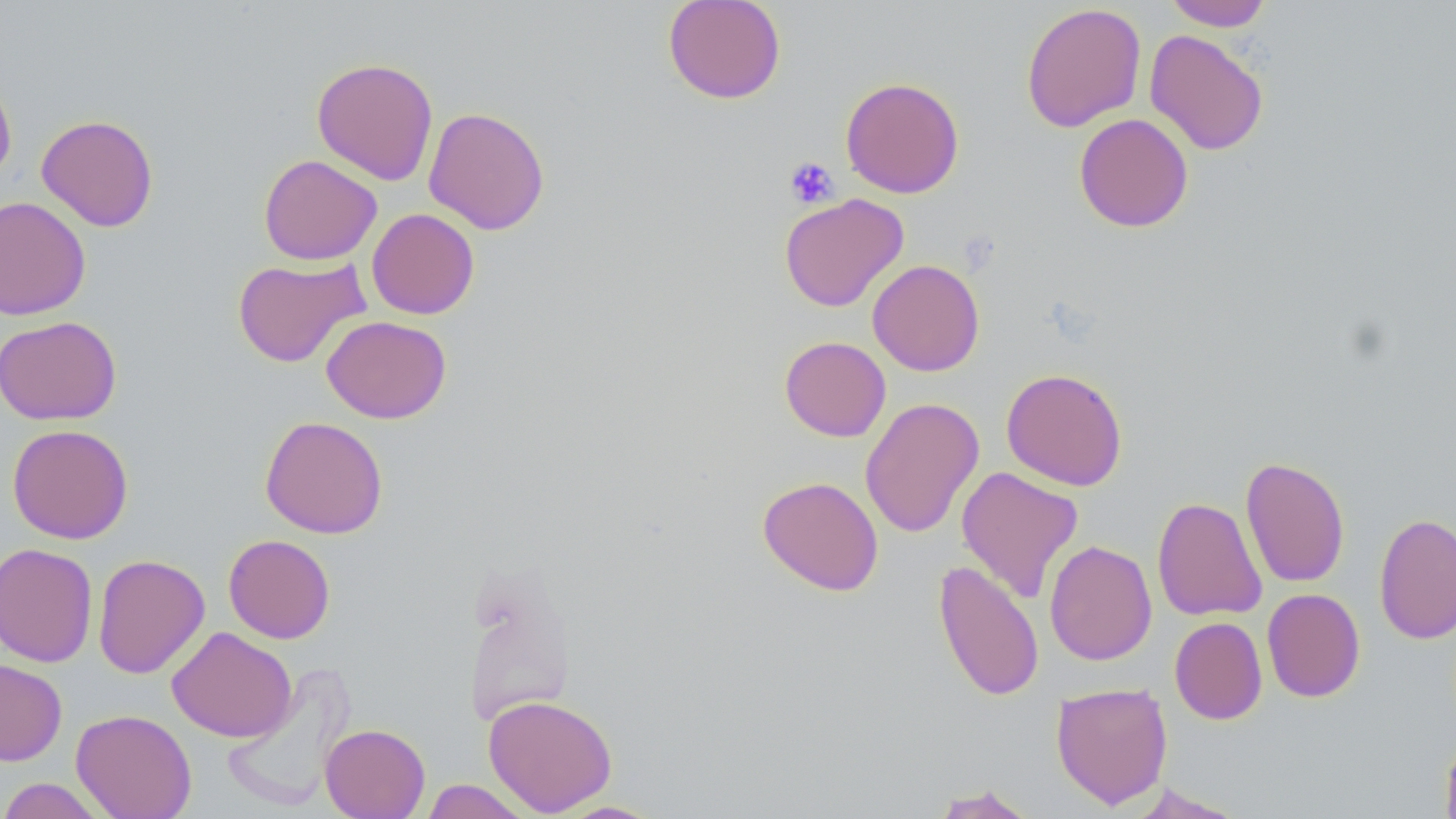
Summary:
  - Coordinate format: approximate bounding boxes as (x1,y1)-(x2,y2) corner pairs in pixels
  - Uninfected red blood cell locations: (662,0)-(786,104), (1163,0)-(1274,31), (1021,2)-(1147,132), (1144,29)-(1270,156), (311,57)-(439,185), (0,72)-(17,185), (840,76)-(965,198), (423,106)-(550,235), (1073,113)-(1194,233), (36,114)-(159,232), (258,154)-(382,265), (779,193)-(909,312), (0,196)-(91,321), (366,208)-(480,319), (232,256)-(369,367), (867,259)-(985,376), (0,315)-(122,425), (321,315)-(452,424), (779,336)-(891,441), (1001,368)-(1128,490), (860,397)-(984,538), (259,415)-(388,539), (7,423)-(133,544), (1240,456)-(1350,588), (956,466)-(1084,603), (757,476)-(884,596), (1152,496)-(1267,621), (1374,512)-(1456,645), (223,534)-(336,643), (1044,540)-(1157,666), (0,542)-(99,668), (92,554)-(210,679), (459,558)-(579,729), (933,560)-(1045,702), (1262,588)-(1366,703), (1169,617)-(1267,725), (167,627)-(297,743), (0,658)-(67,766), (222,668)-(355,812), (1051,681)-(1173,809), (483,694)-(617,816), (71,709)-(197,819), (320,723)-(430,819), (1440,733)-(1456,819), (0,777)-(109,818), (420,779)-(531,818), (1126,783)-(1245,818), (929,784)-(1039,818), (552,800)-(665,818)
  - Platelet locations: (784,156)-(839,208)
  - Slide-level diagnosis: negative for blood parasites
  - Preparation: thin blood film
  - Modality: light microscopy
  - Magnification: 1000x
  - Stain: May-Grünwald-Giemsa
  - Image size: 1456×819 pixels
  - Field of view: single